Identify the parasite.
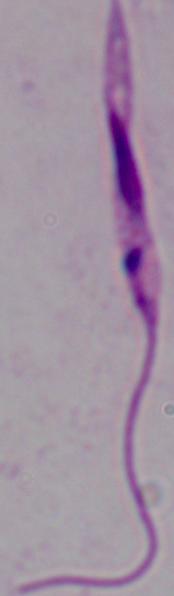

This is Leishmania.

magnification: 1000x
modality: micrograph